Name the parasite shown.
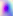
This is Toxoplasma gondii.

400x magnification. Micrograph.